Give the position of every leukocyte visible.
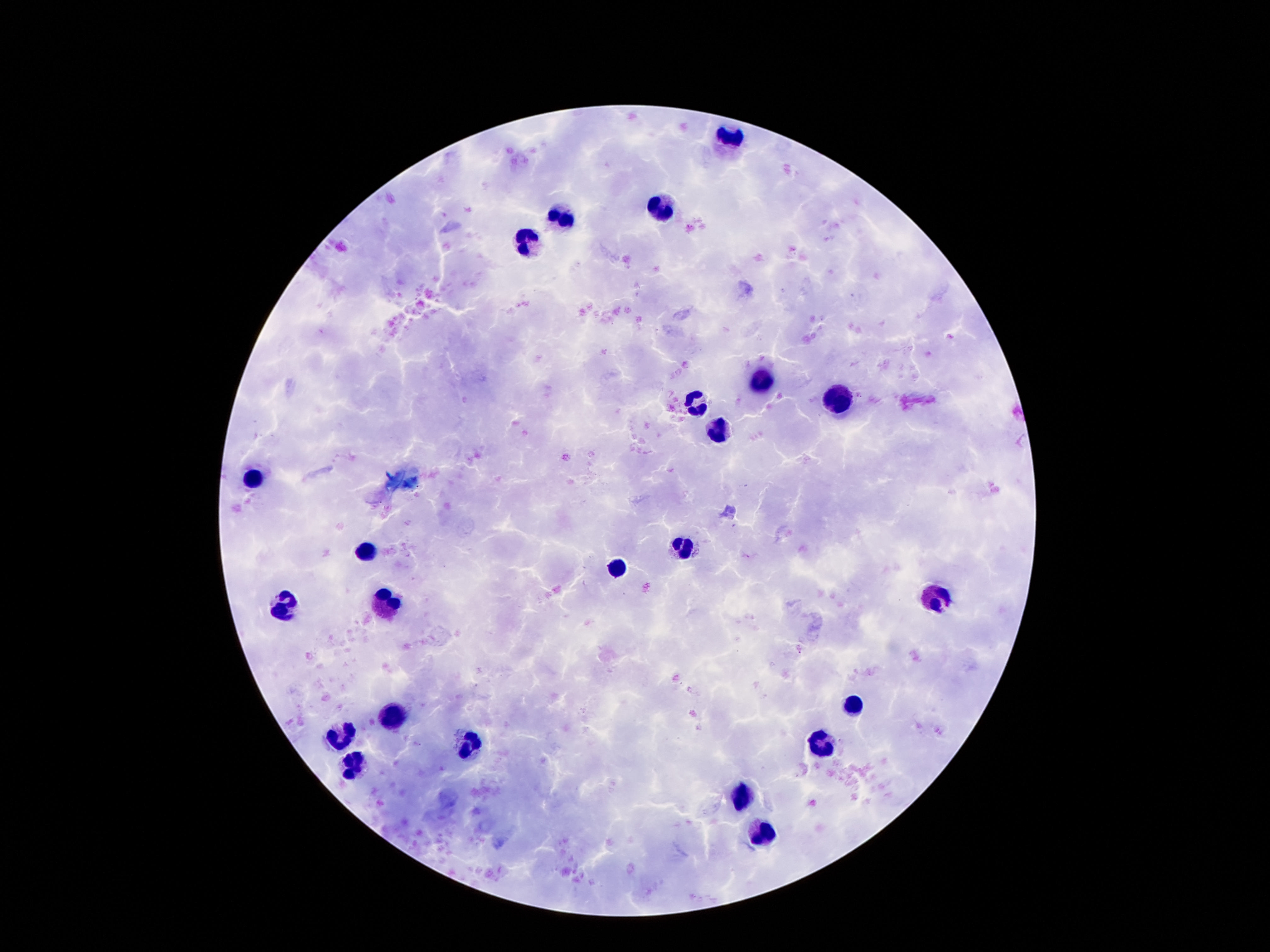
Approximate centers as (x, y) in pixels.
Leukocytes: (730, 136), (664, 209), (562, 219), (527, 244), (761, 380), (836, 402), (695, 404), (716, 434), (251, 480), (683, 544), (365, 554), (617, 564), (933, 599), (386, 602), (281, 609), (853, 705), (394, 718), (341, 732), (822, 742), (470, 744), (355, 769), (742, 795), (763, 832).

patient malaria status = uninfected
stain = Giemsa
image size = 1270×952 pixels
field of view = one from this slide
capture = smartphone camera through the microscope eyepiece
preparation = thick blood smear
magnification = 100x